Assess for parasitized red blood cells.
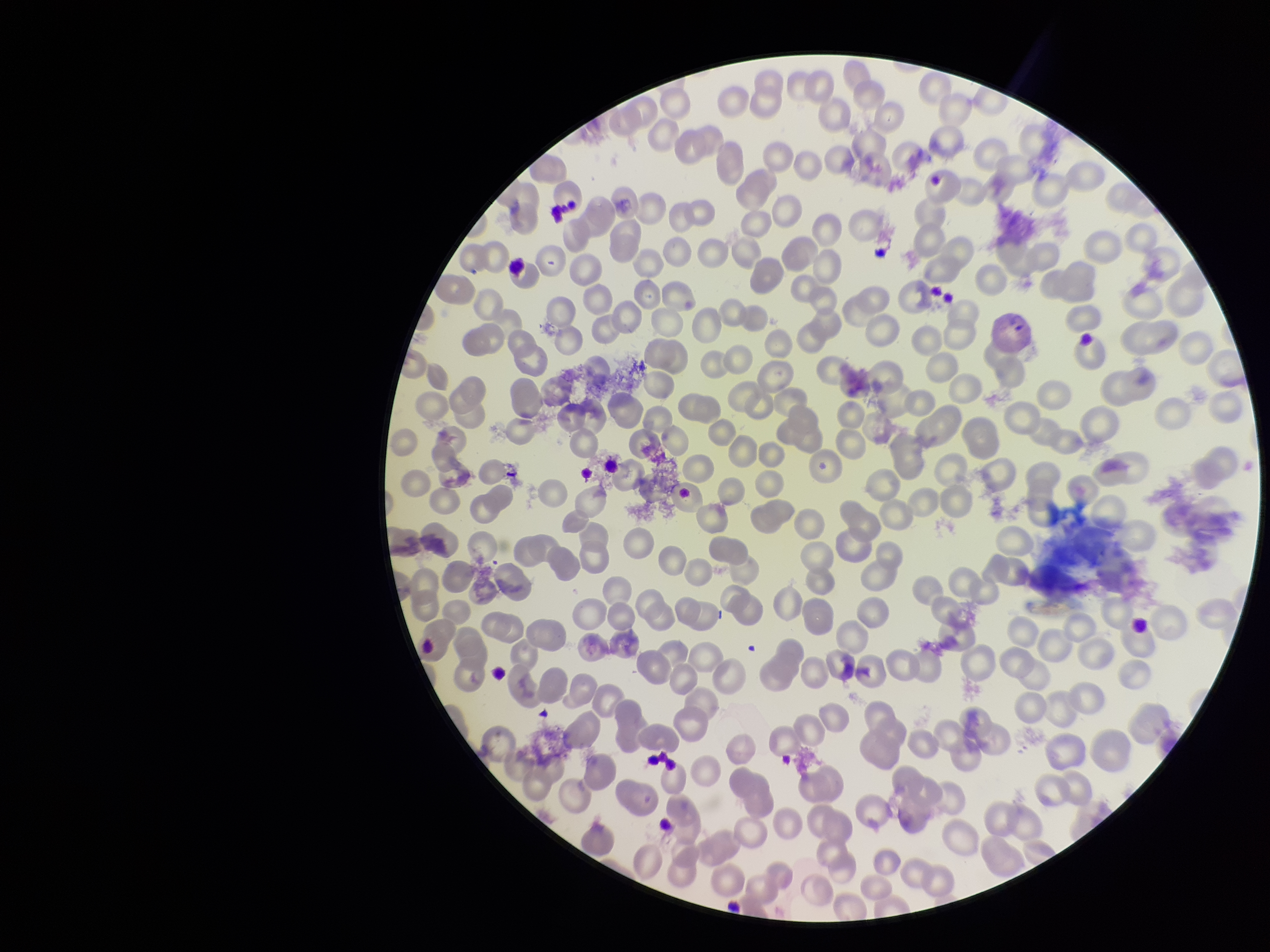

None identified.

capture = smartphone photograph through the microscope eyepiece
patient malaria status = positive
preparation = thin
red blood cell count = 247
species reported for this patient = Plasmodium vivax
parasitized red blood cell count = 0
stain = Giemsa
field of view = one from this slide
image size = 1270×952 pixels